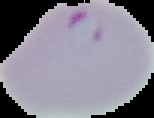
image type = segmented cell region with the area outside set to black
preparation = thin blood smear
malaria status = parasitized
image size = 154×118 pixels